Outline each blood parasite and name the species.
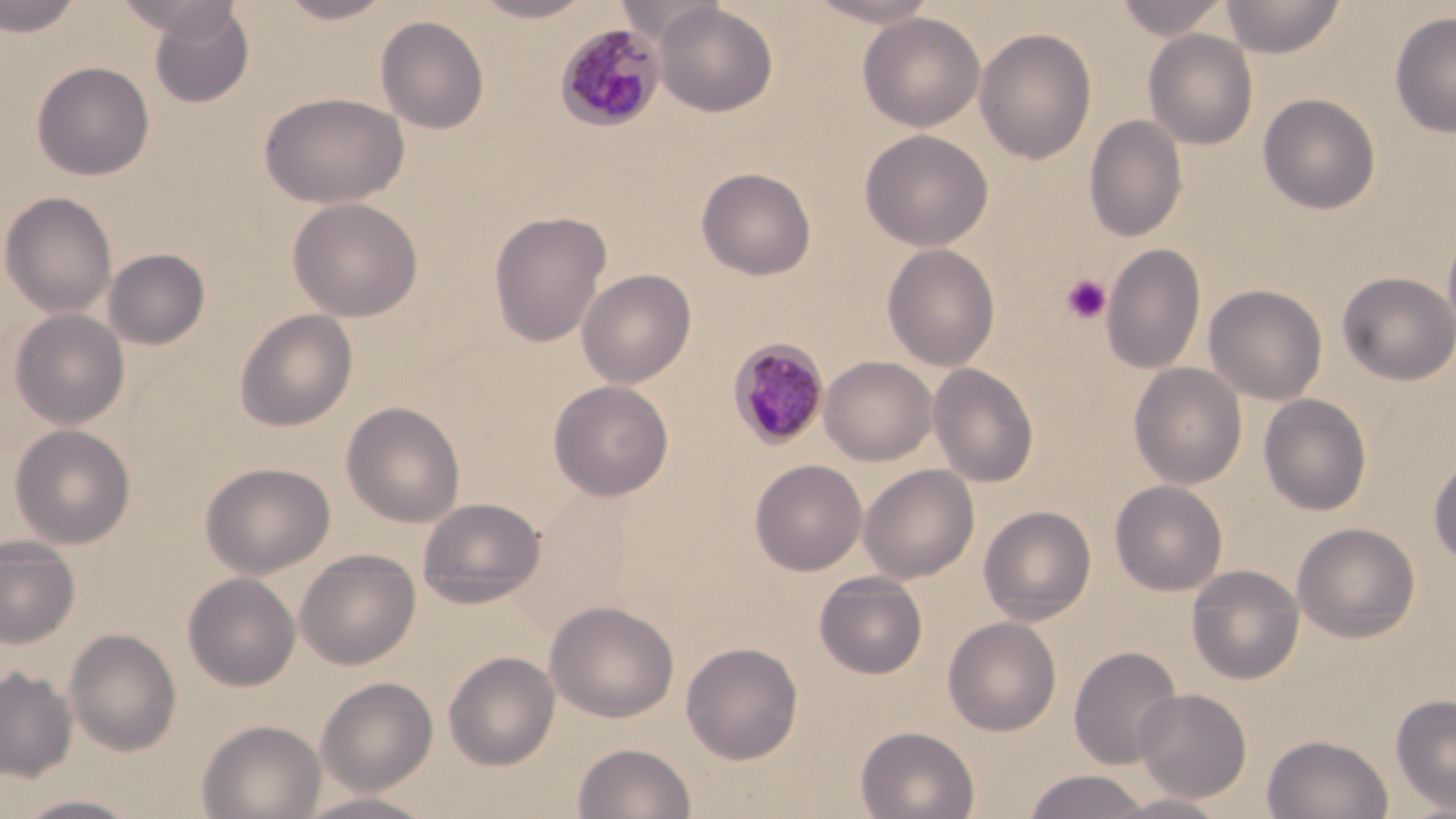
Approximate bounding boxes as named x1/y1/x2/y2 corners in pixels.
Plasmodium malariae-infected red blood cells: (x1=554, y1=22, x2=667, y2=131), (x1=727, y1=337, x2=830, y2=451).
No Plasmodium falciparum, Plasmodium ovale, Plasmodium vivax, Babesia divergens, or Trypanosoma brucei observed.

Summary:
  - Uninfected red blood cell locations: (x1=0, y1=0, x2=85, y2=37), (x1=115, y1=0, x2=241, y2=43), (x1=274, y1=0, x2=395, y2=23), (x1=471, y1=0, x2=595, y2=22), (x1=612, y1=0, x2=726, y2=44), (x1=804, y1=0, x2=942, y2=27), (x1=1114, y1=0, x2=1232, y2=41), (x1=1221, y1=0, x2=1346, y2=58), (x1=653, y1=2, x2=778, y2=117), (x1=148, y1=4, x2=256, y2=108), (x1=858, y1=12, x2=985, y2=132), (x1=1389, y1=12, x2=1456, y2=138), (x1=375, y1=15, x2=490, y2=134), (x1=974, y1=27, x2=1097, y2=165), (x1=1143, y1=29, x2=1258, y2=150), (x1=31, y1=61, x2=154, y2=180), (x1=258, y1=91, x2=409, y2=209), (x1=1257, y1=93, x2=1381, y2=215), (x1=1084, y1=114, x2=1188, y2=242), (x1=859, y1=128, x2=994, y2=251), (x1=696, y1=167, x2=817, y2=280), (x1=1, y1=191, x2=117, y2=318), (x1=287, y1=197, x2=423, y2=321), (x1=488, y1=211, x2=612, y2=347), (x1=1442, y1=224, x2=1456, y2=349), (x1=1101, y1=242, x2=1206, y2=374), (x1=882, y1=243, x2=1000, y2=371), (x1=103, y1=248, x2=211, y2=350), (x1=576, y1=268, x2=697, y2=389), (x1=1336, y1=272, x2=1456, y2=385), (x1=1204, y1=284, x2=1328, y2=405), (x1=8, y1=308, x2=130, y2=429), (x1=233, y1=309, x2=358, y2=432), (x1=820, y1=356, x2=938, y2=466), (x1=1129, y1=362, x2=1247, y2=489), (x1=928, y1=363, x2=1039, y2=487), (x1=547, y1=379, x2=674, y2=501), (x1=1259, y1=394, x2=1372, y2=516), (x1=341, y1=401, x2=465, y2=527), (x1=9, y1=424, x2=136, y2=549), (x1=1428, y1=453, x2=1456, y2=568), (x1=749, y1=459, x2=867, y2=576), (x1=200, y1=461, x2=336, y2=579), (x1=859, y1=464, x2=979, y2=583), (x1=1110, y1=480, x2=1227, y2=596), (x1=417, y1=497, x2=546, y2=608), (x1=978, y1=505, x2=1097, y2=625), (x1=1292, y1=522, x2=1420, y2=643), (x1=0, y1=536, x2=80, y2=649), (x1=295, y1=549, x2=420, y2=670), (x1=1186, y1=564, x2=1304, y2=684), (x1=814, y1=571, x2=928, y2=679), (x1=183, y1=572, x2=301, y2=691), (x1=545, y1=600, x2=680, y2=723), (x1=943, y1=616, x2=1062, y2=735), (x1=64, y1=628, x2=182, y2=756), (x1=681, y1=641, x2=803, y2=764), (x1=1067, y1=645, x2=1183, y2=770), (x1=443, y1=651, x2=560, y2=771), (x1=0, y1=668, x2=78, y2=782), (x1=316, y1=677, x2=438, y2=796), (x1=1134, y1=688, x2=1253, y2=803), (x1=1391, y1=693, x2=1456, y2=814), (x1=197, y1=718, x2=326, y2=819), (x1=855, y1=726, x2=979, y2=819), (x1=1261, y1=734, x2=1394, y2=819), (x1=572, y1=742, x2=697, y2=819), (x1=1022, y1=769, x2=1153, y2=818), (x1=295, y1=791, x2=440, y2=818), (x1=1104, y1=792, x2=1233, y2=818), (x1=13, y1=794, x2=144, y2=818)
  - Platelet locations: (x1=1061, y1=274, x2=1112, y2=326)
  - Slide-level diagnosis: Plasmodium malariae
  - Preparation: thin blood smear
  - Field of view: single
  - Image size: 1456×819 pixels
  - Stain: May-Grünwald-Giemsa
  - Modality: optical microscopy
  - Magnification: 1000x